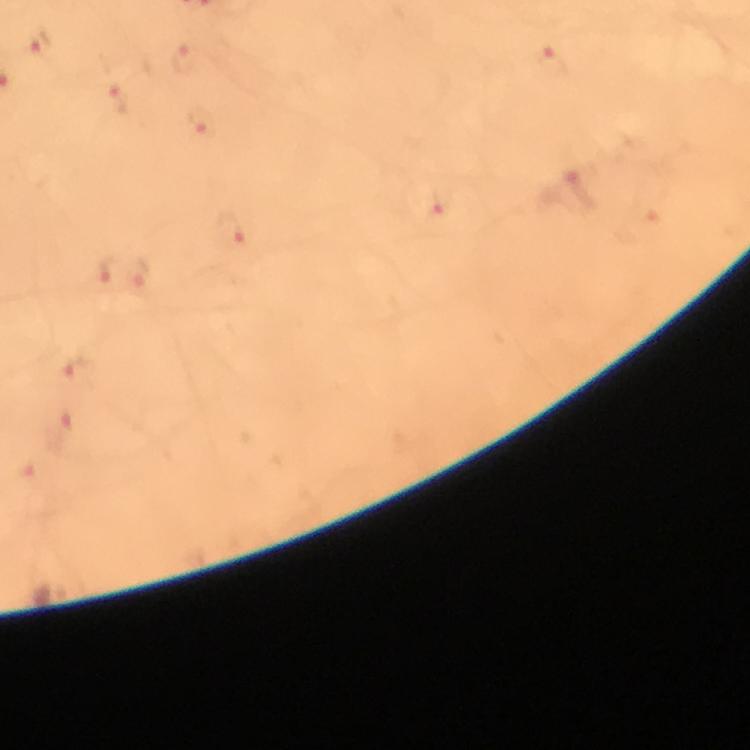

Approximate centers as (x, y) in pixels. Plasmodium parasite locations: (40, 43), (183, 58), (551, 63), (116, 99), (201, 123), (577, 186), (438, 206), (230, 230), (104, 270), (140, 277), (76, 373), (60, 432). Smartphone photograph taken through a microscope. Thick blood smear. A crop from one field of view. Immersion oil was used. 100x magnification. Image is 750×750 pixels. From a diagnostic examination for malaria. Giemsa stain.